Comment on the morphology of the erythrocytes.
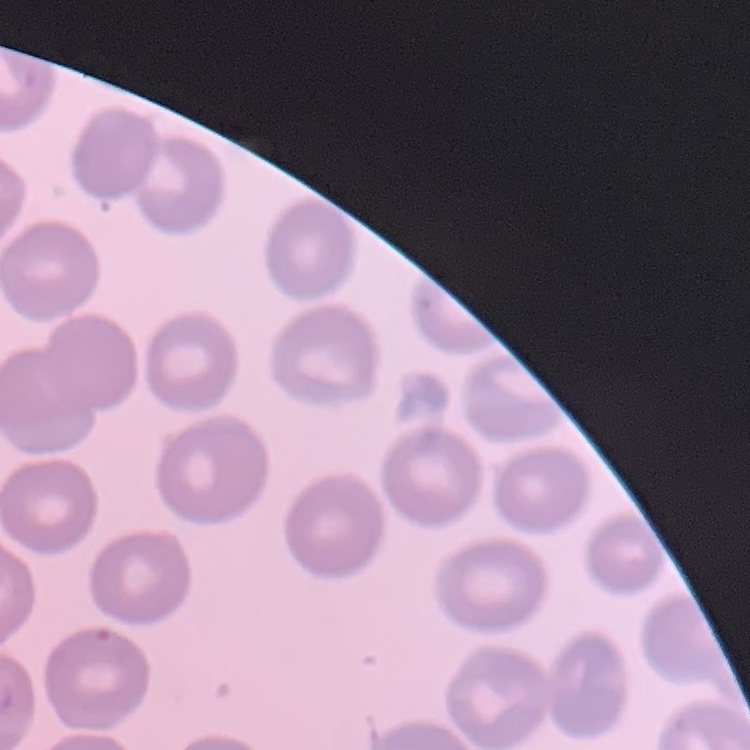

They show no rouleaux formation.

One tile cut from a larger photomicrograph. Thin blood film. Stained with either Field's or Giemsa.